Evaluate for malaria.
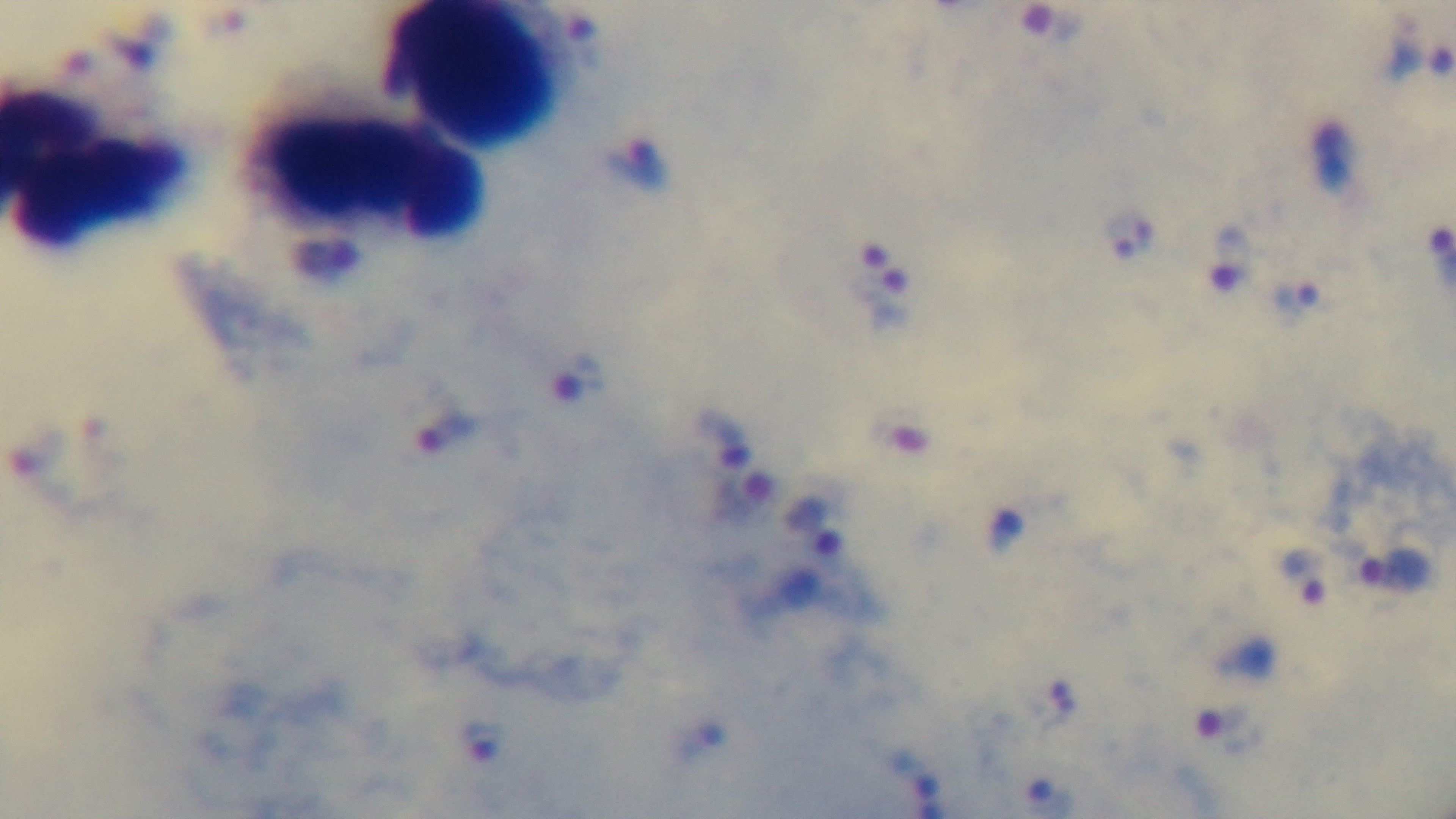

It is infected.

{
  "stain": "Giemsa",
  "objective": "100x oil immersion",
  "field_of_view": "one from the slide",
  "preparation": "thick smear",
  "modality": "light microscopy",
  "capture": "mounted 4K digital camera"
}